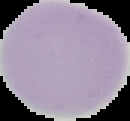 Cell region segmented out of the field of view; the surrounding area is masked to black. From a thin blood smear. Image is 130×121 pixels. Malaria status: uninfected.